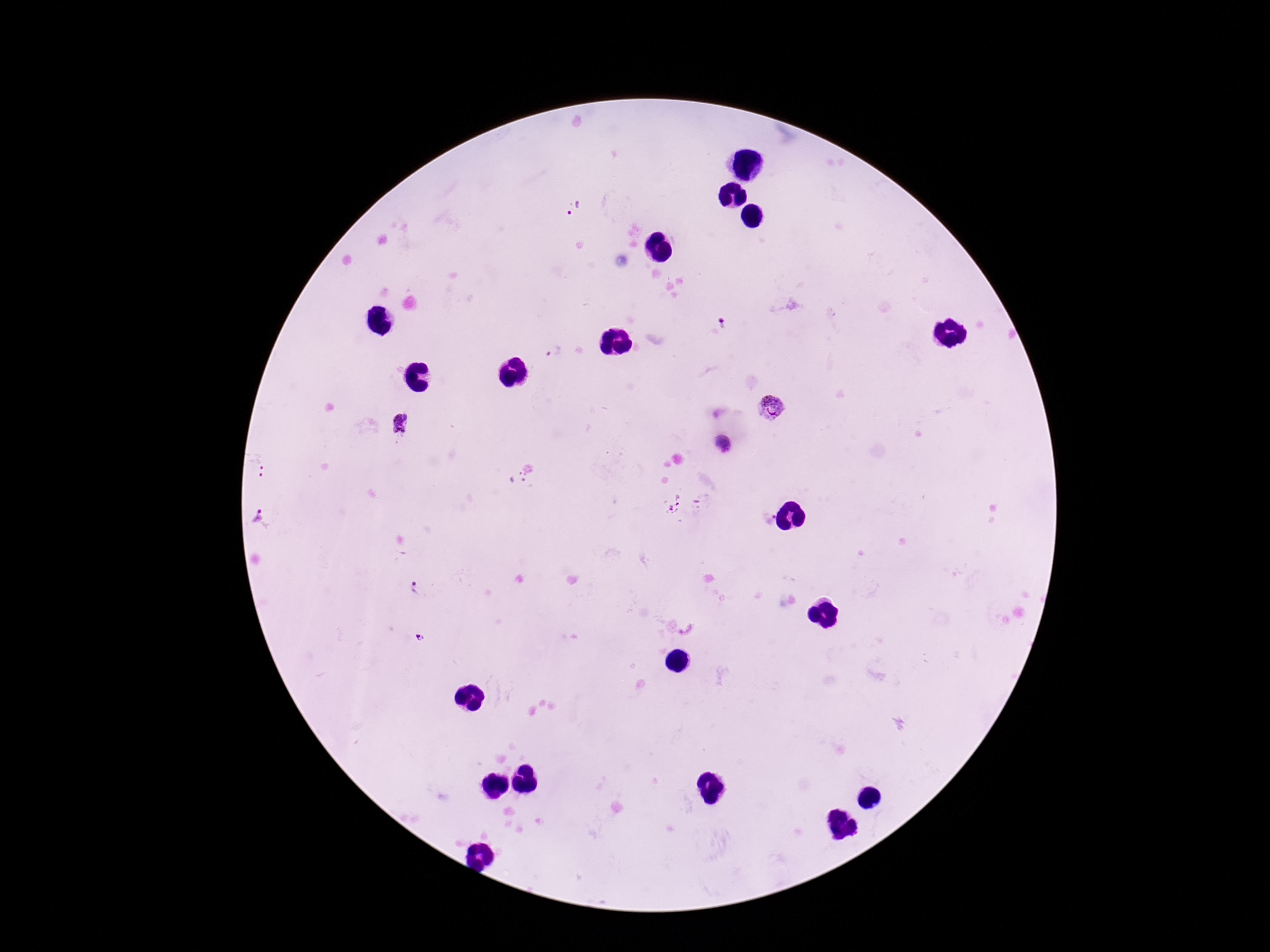

Approximate centers as (x, y) in pixels. Plasmodium parasite locations: (574, 209), (718, 325), (554, 352), (772, 407), (403, 427), (723, 445), (517, 479), (675, 503), (257, 518), (417, 590), (689, 629), (421, 637). Patient malaria status: positive. Giemsa-stained preparation. Image is 1270×952 pixels. 100x magnification. Thick blood smear. Single field of view. Smartphone photograph taken through the microscope eyepiece.